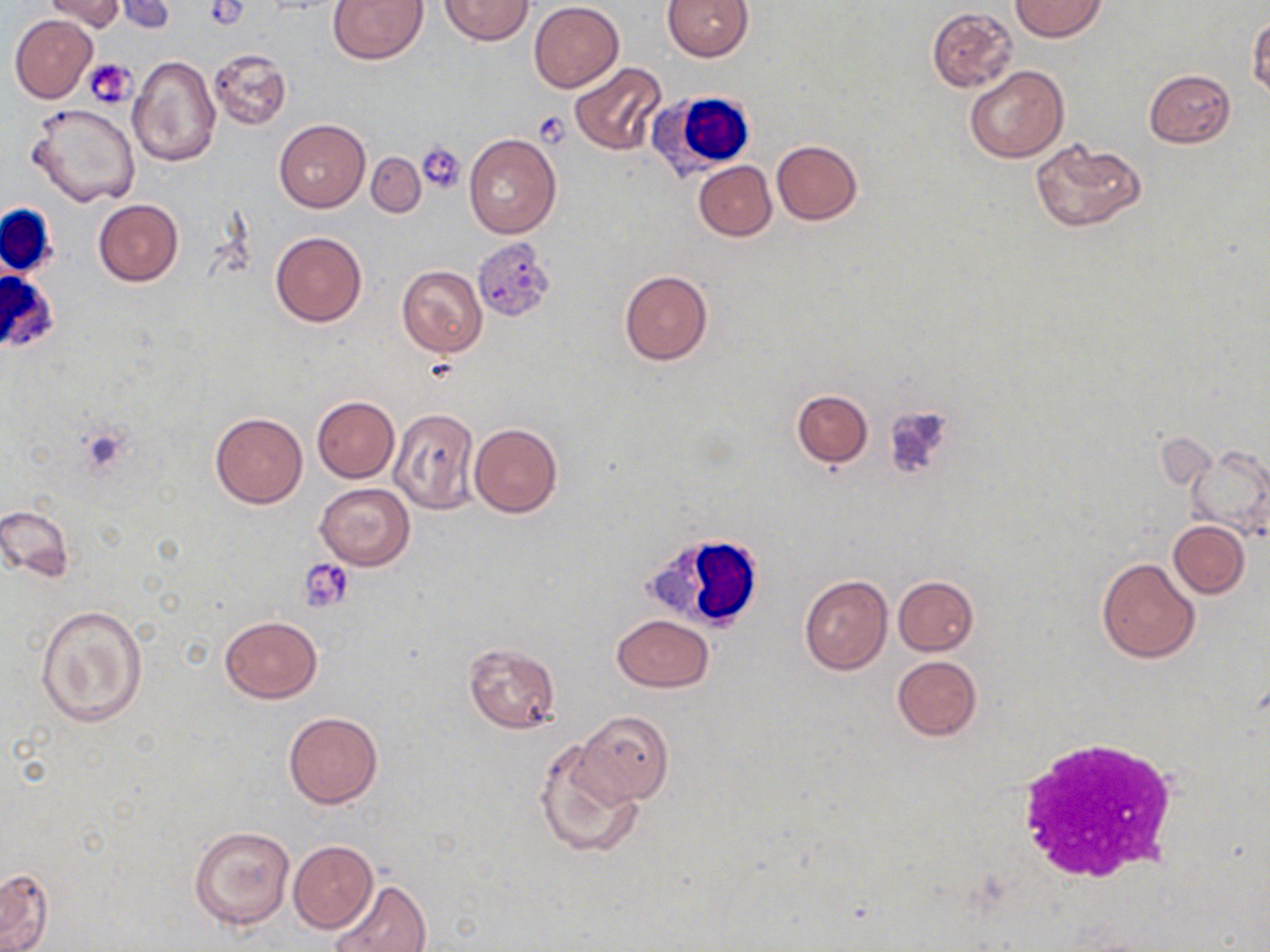
Summary:
  - Coordinate format: approximate bounding boxes as (x1, y1, x2, y2) in pixels
  - Platelet locations: (86, 59, 137, 109), (535, 111, 572, 147), (419, 142, 466, 192), (423, 356, 459, 381), (300, 559, 355, 612)
  - Uninfected red blood cell locations: (112, 0, 177, 34), (327, 0, 427, 64), (439, 0, 535, 46), (662, 0, 754, 61), (1010, 0, 1107, 41), (40, 1, 127, 34), (530, 1, 623, 91), (928, 7, 1017, 91), (1247, 14, 1269, 99), (10, 15, 97, 102), (206, 48, 291, 129), (128, 56, 221, 167), (570, 61, 667, 155), (965, 66, 1068, 163), (1144, 69, 1235, 148), (27, 103, 141, 206), (274, 119, 369, 212), (464, 133, 561, 239), (1029, 139, 1146, 233), (771, 140, 862, 225), (366, 153, 425, 218), (693, 161, 776, 240), (93, 199, 184, 286), (271, 232, 366, 327), (397, 266, 487, 357), (620, 272, 713, 365), (792, 389, 872, 468), (312, 396, 399, 482), (388, 407, 479, 514), (210, 411, 306, 508), (469, 423, 562, 517), (1184, 445, 1270, 543), (315, 483, 414, 569), (0, 503, 75, 583), (1169, 520, 1249, 597), (1096, 556, 1202, 663), (799, 575, 892, 674), (893, 576, 978, 655), (35, 605, 148, 727), (611, 615, 715, 691), (219, 616, 322, 704), (462, 642, 560, 733), (892, 655, 982, 740), (576, 711, 673, 805), (283, 712, 383, 808), (536, 739, 643, 859), (189, 824, 296, 929), (289, 840, 378, 932), (0, 867, 54, 952), (326, 879, 433, 952)
  - White blood cell locations: (647, 92, 757, 179), (1, 202, 58, 281), (1, 268, 59, 354), (644, 529, 769, 632), (1012, 737, 1182, 886)
  - Slide-level diagnosis: negative for blood parasites
  - Image size: 1270×952 pixels
  - Field of view: one of a larger specimen
  - Magnification: 1000x
  - Stain: May-Grünwald-Giemsa
  - Modality: optical microscopy
  - Preparation: thin blood smear